State which parasite is depicted.
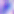

This is Toxoplasma gondii.

Micrograph. 400x magnification.